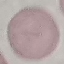

Summary:
  - Malaria status: uninfected
  - Stain: Giemsa
  - Preparation: thin blood film
  - Capture: smartphone through the microscope eyepiece
  - Image type: automatically extracted cell patch, resized to 64 × 64 pixels